Assess the morphology of the erythrocytes.
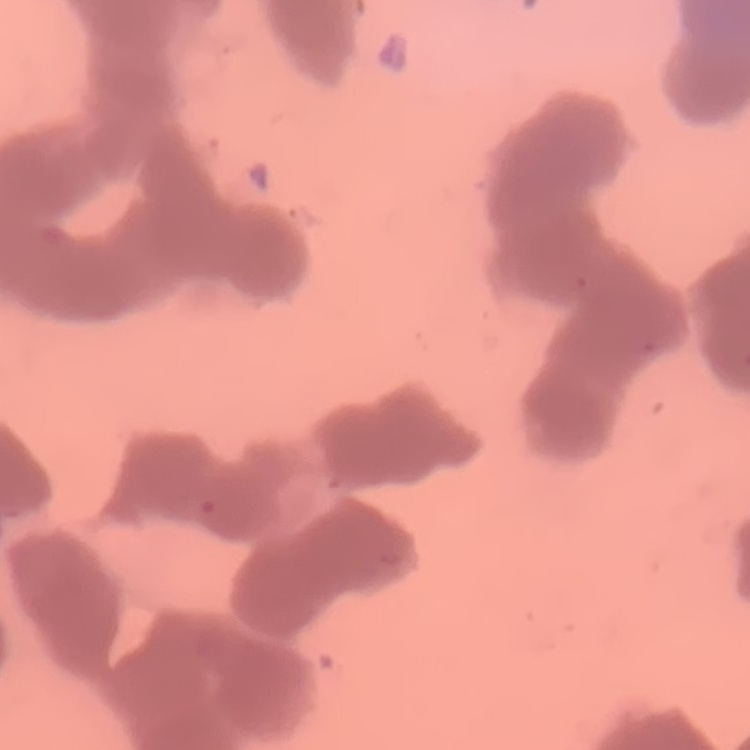
They show rouleaux formation.

Thin peripheral smear. One tile cut from a larger photomicrograph. Field's or Giemsa stain.